Assess the morphology of the erythrocytes.
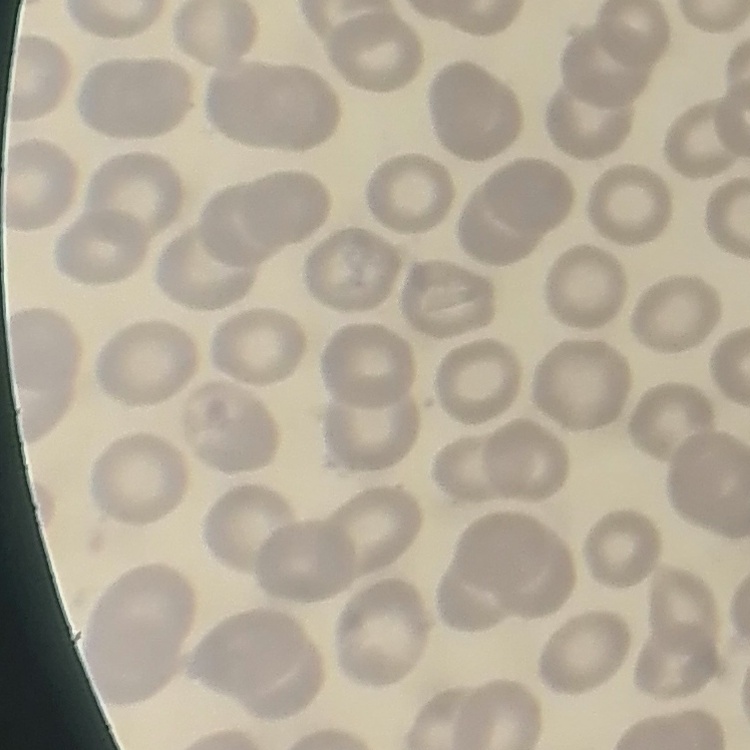
No rouleaux formation.

Summary:
  - Stain: Field's or Giemsa
  - Preparation: thin blood smear
  - Image type: square crop of a larger photomicrograph